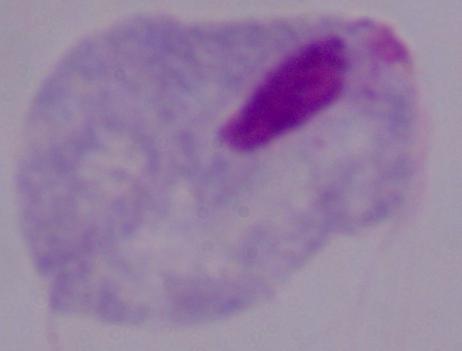

modality = micrograph
magnification = 1000x
identification = trichomonad